State which parasite is depicted.
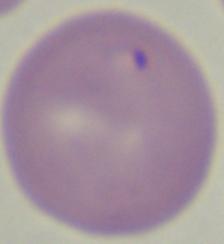
This is Babesia.

{
  "modality": "micrograph",
  "magnification": "1000x"
}